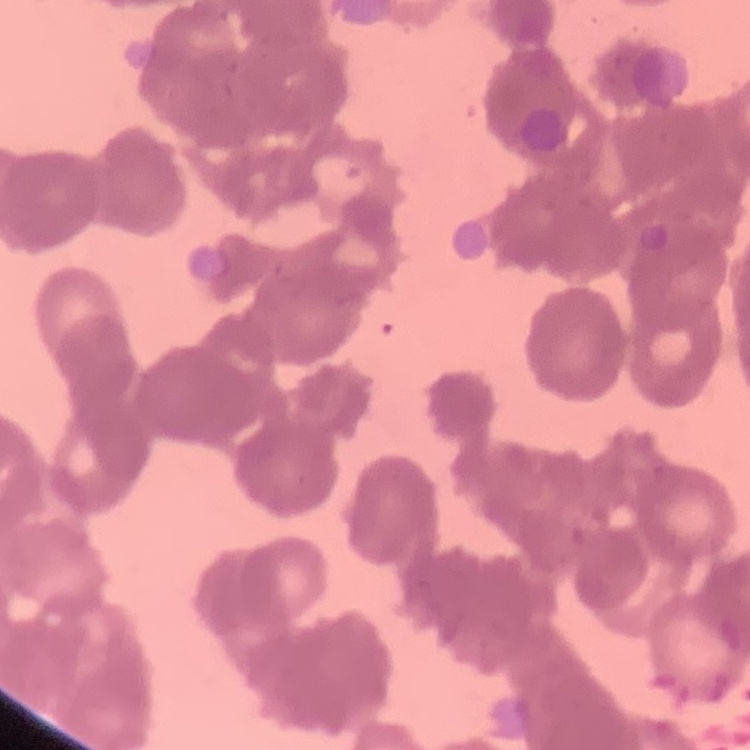

red blood cell morphology = rouleaux formation
image type = square crop of a larger photomicrograph
preparation = thin blood film
stain = Field's or Giemsa